Assess the morphology of the erythrocytes.
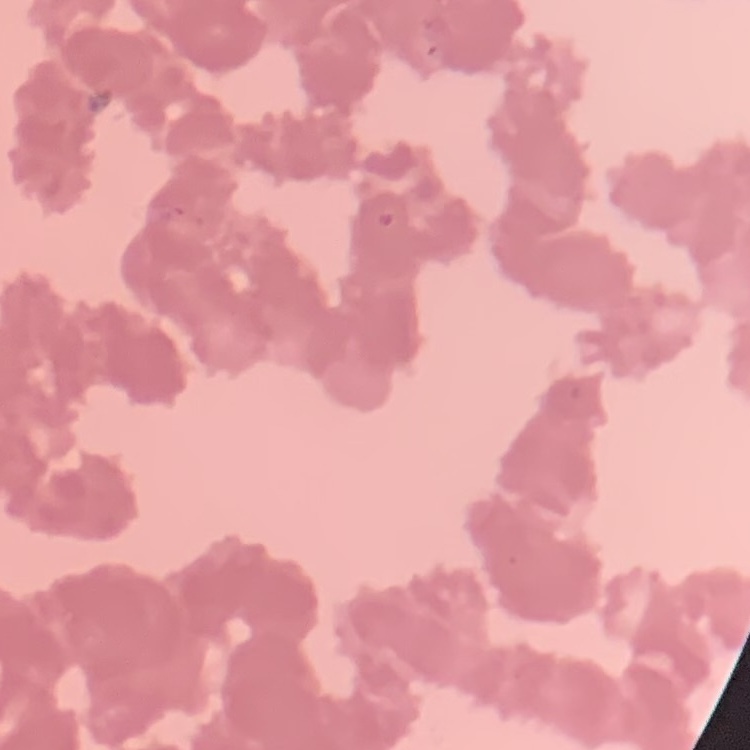
Rouleaux formation.

stain = Field's or Giemsa
preparation = thin blood smear
image type = square crop of a larger photomicrograph